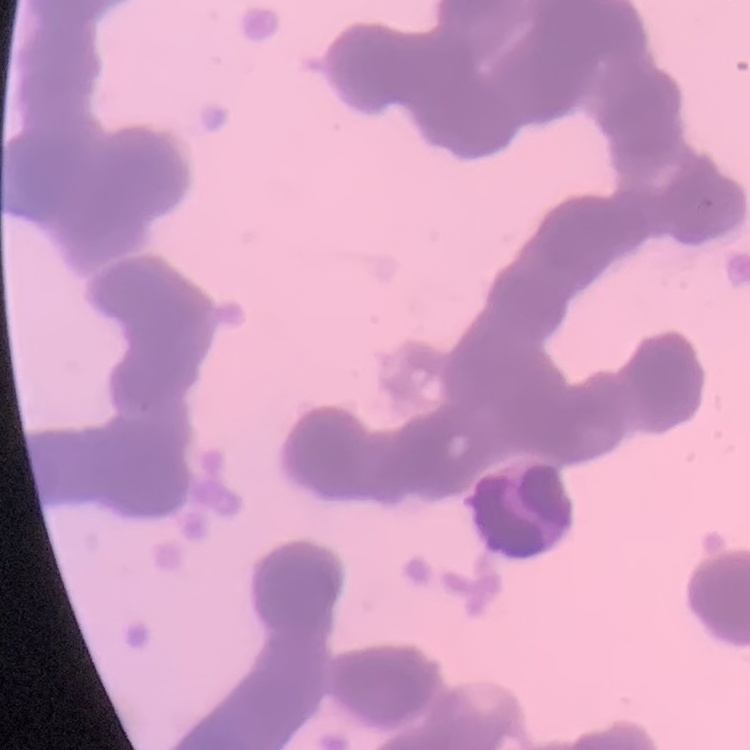

erythrocyte morphology = rouleaux formation
stain = Field's or Giemsa
preparation = thin blood film
image type = one tile cut from a larger photomicrograph